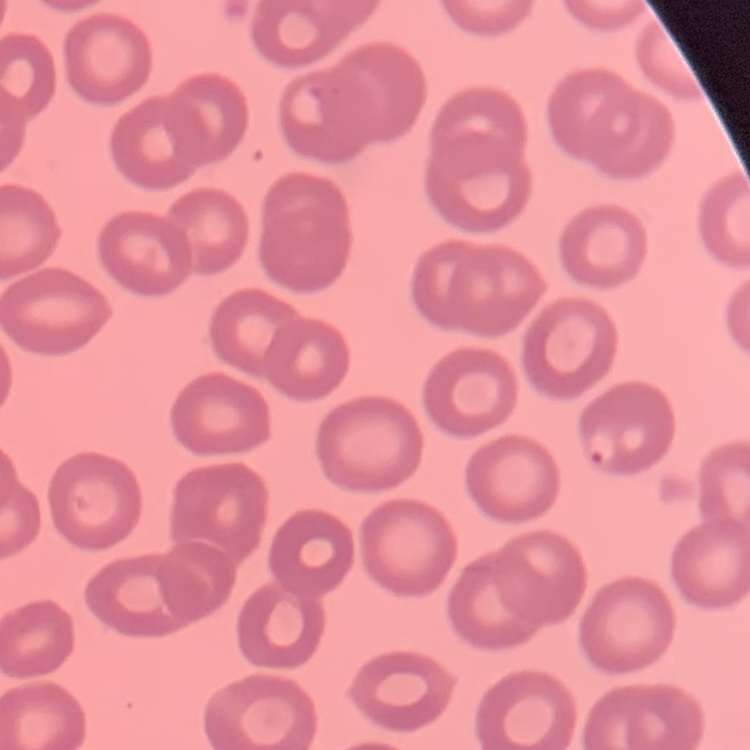

red blood cell morphology = no rouleaux formation
image type = square crop of a larger photomicrograph
preparation = thin peripheral smear
stain = Field's or Giemsa